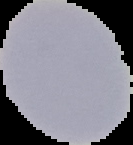

{
  "preparation": "thin blood film",
  "result": "negative for Plasmodium parasites",
  "image_type": "segmented cell region with the area outside set to black",
  "image_size": "133×145 pixels"
}